Locate and identify every blood parasite.
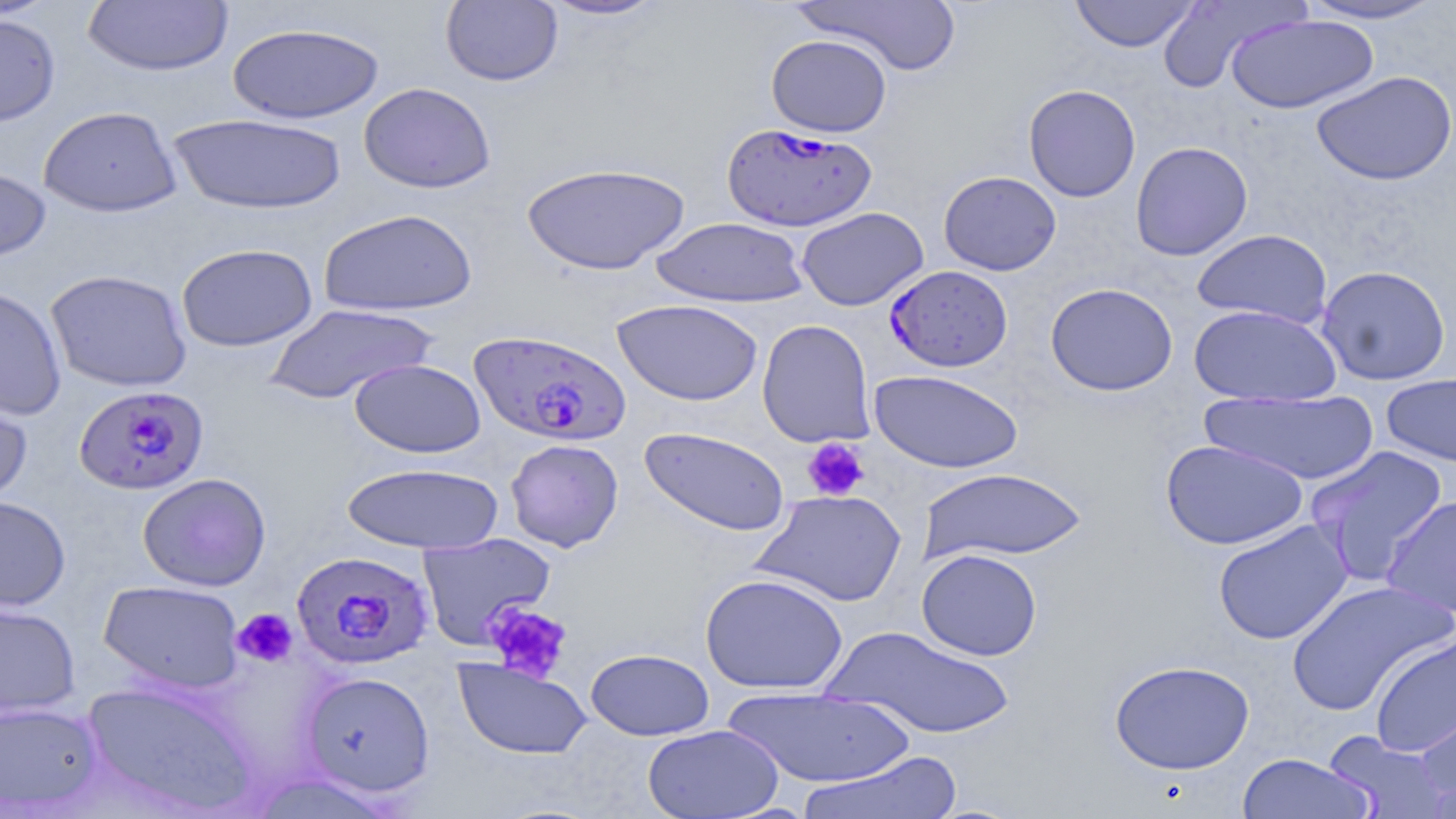
Approximate bounding boxes as (x1, y1, x2, y2) in pixels.
Plasmodium falciparum-infected red blood cells: (720, 122, 877, 232), (884, 265, 1013, 372), (469, 329, 632, 446), (74, 385, 208, 495), (291, 550, 434, 670).
No Plasmodium ovale, Plasmodium malariae, Plasmodium vivax, Babesia divergens, or Trypanosoma brucei observed.

Uninfected red blood cell locations: (535, 0, 673, 22), (793, 0, 963, 76), (1069, 0, 1200, 52), (1156, 0, 1306, 93), (1296, 0, 1448, 25), (83, 1, 234, 77), (440, 1, 563, 86), (0, 13, 60, 126), (1226, 14, 1378, 114), (227, 23, 385, 124), (766, 34, 892, 137), (1311, 70, 1456, 186), (358, 82, 496, 193), (1023, 84, 1141, 202), (38, 106, 183, 217), (168, 113, 347, 215), (1130, 141, 1253, 261), (521, 162, 690, 275), (0, 164, 52, 266), (938, 170, 1061, 275), (796, 206, 929, 310), (318, 208, 477, 317), (651, 216, 809, 308), (1191, 229, 1333, 328), (176, 243, 318, 351), (1316, 264, 1451, 386), (45, 269, 192, 393), (1045, 282, 1178, 396), (0, 286, 67, 420), (612, 298, 763, 406), (264, 303, 437, 404), (1188, 304, 1342, 406), (756, 319, 875, 448), (349, 358, 486, 458), (868, 369, 1024, 474), (1380, 372, 1456, 468), (0, 379, 33, 509), (1200, 390, 1380, 485), (639, 426, 790, 536), (504, 438, 624, 552), (1160, 439, 1308, 551), (1304, 445, 1449, 584), (340, 461, 504, 554), (918, 468, 1088, 563), (137, 472, 271, 591), (753, 488, 908, 607), (0, 496, 70, 612), (1381, 496, 1455, 622), (1213, 519, 1353, 645), (416, 533, 556, 649), (916, 549, 1042, 661), (699, 573, 849, 694), (1286, 579, 1454, 716), (98, 580, 245, 694), (0, 601, 81, 719), (823, 625, 1016, 740), (1369, 633, 1456, 759), (586, 648, 714, 741), (453, 658, 592, 760), (1109, 659, 1255, 775), (300, 671, 435, 797), (80, 677, 260, 816), (723, 687, 911, 788), (1414, 694, 1456, 810), (0, 700, 105, 814), (642, 724, 784, 818), (1323, 731, 1450, 819), (797, 750, 963, 819), (1236, 753, 1374, 818). Platelet locations: (802, 438, 870, 501), (481, 601, 573, 684), (232, 607, 298, 668). Slide-level diagnosis: Plasmodium falciparum. Optical microscopy. One field of a larger specimen. May-Grünwald-Giemsa stain. Captured at 1000x magnification. Thin blood film. Image is 1456×819 pixels.